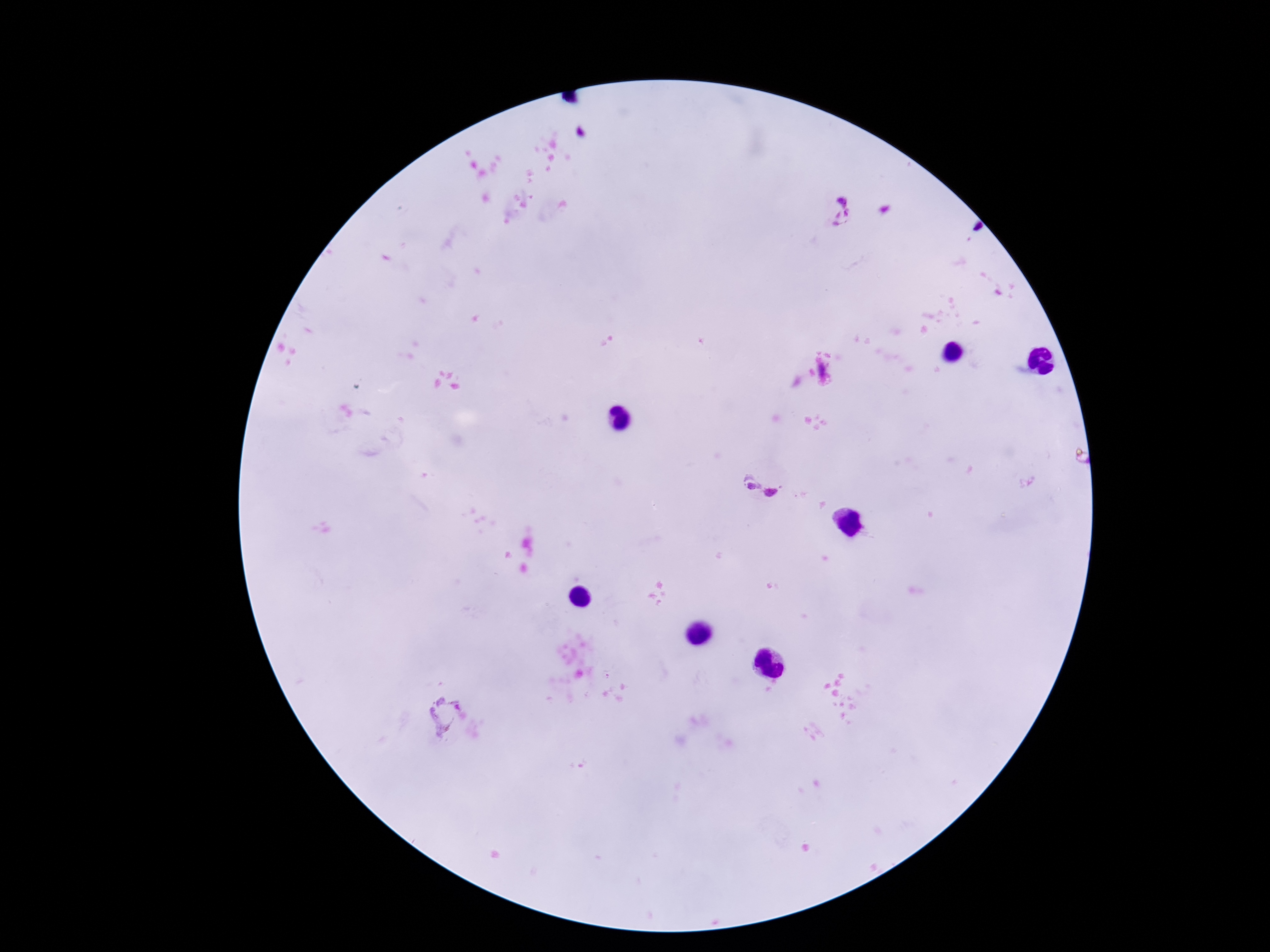

Approximate centers as {x, y} in pixels. Plasmodium parasite locations: {841, 212}, {751, 483}, {771, 493}, {444, 713}. Photographed through the microscope eyepiece with a smartphone camera. Image is 1270×952 pixels. Thick blood smear. 100x magnification. Patient malaria status: positive. Giemsa stain. One field from this slide.